Identify the cell.
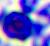

This is a leukocyte.

magnification = 400x
modality = photomicrograph